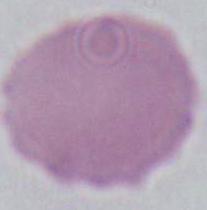
Summary:
  - Modality: micrograph
  - Identification: erythrocyte
  - Magnification: 1000x